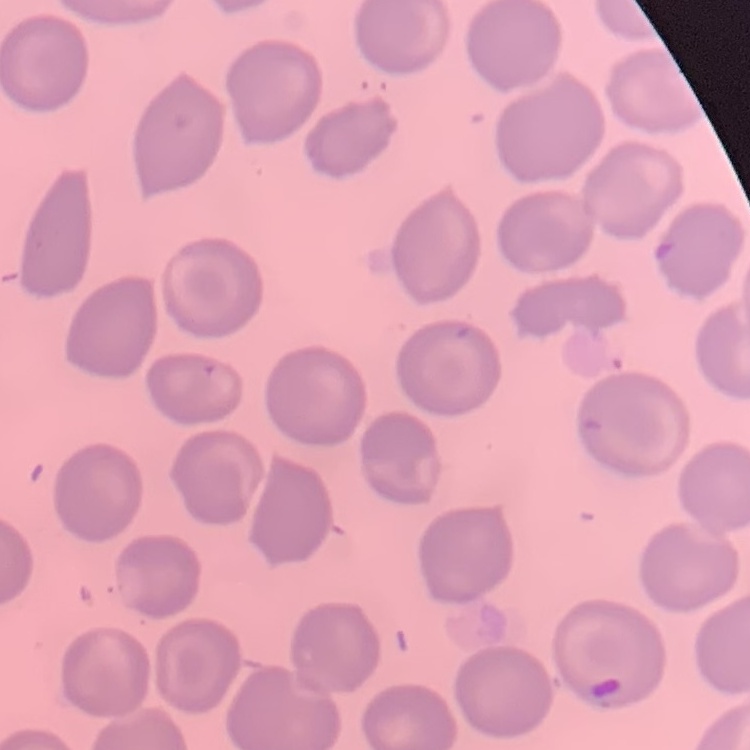

Summary:
  - Erythrocyte morphology: no rouleaux formation
  - Image type: one tile cut from a larger photomicrograph
  - Preparation: thin blood smear
  - Stain: Field's or Giemsa